Look for Plasmodium parasites.
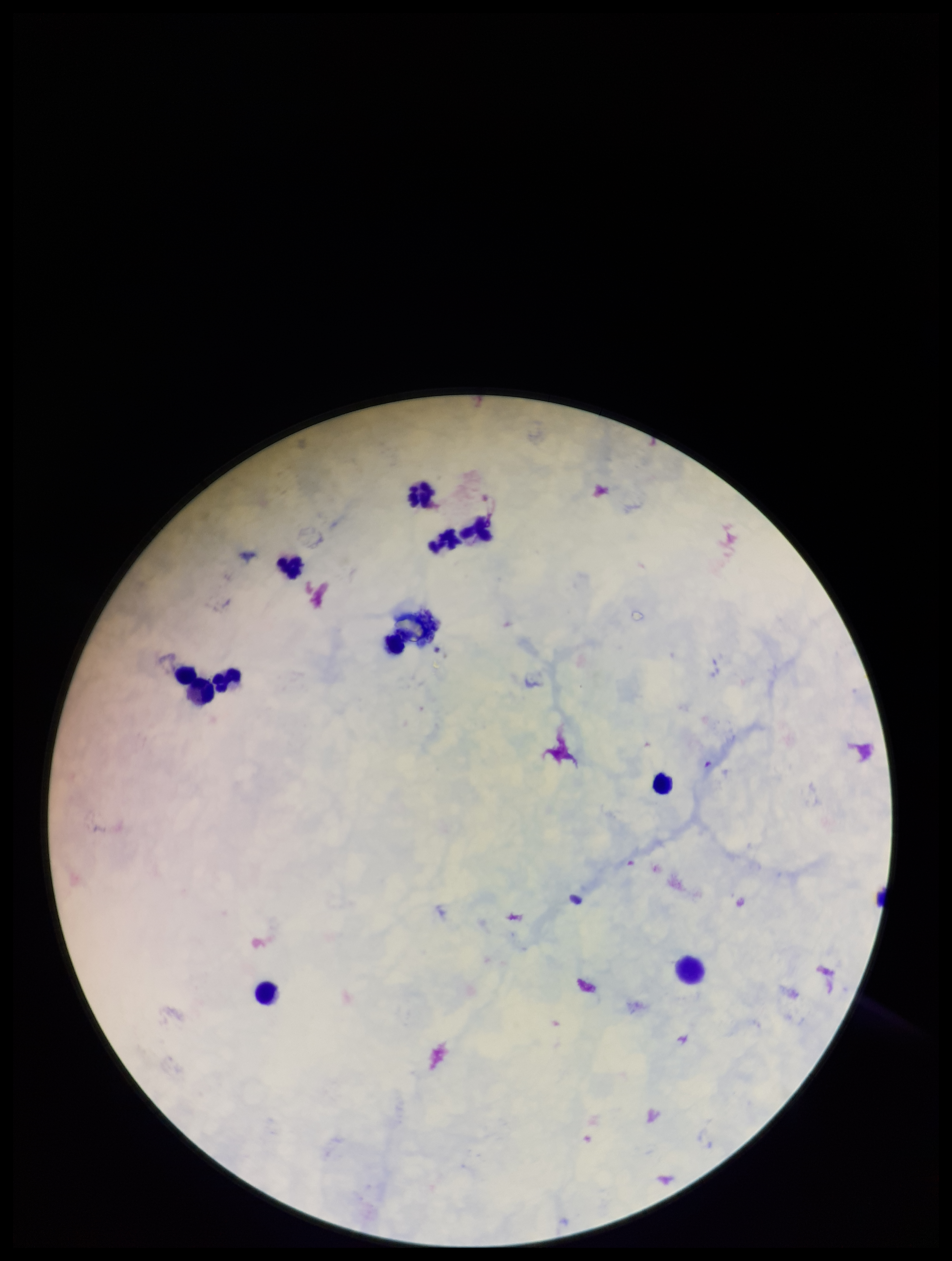
None identified.

Single field of view. Image is 952×1261 pixels. Photographed through the microscope eyepiece with a smartphone camera. Leukocyte count: 10. Preparation: thick blood smear. Parasite count: 0. Stained with Giemsa. Patient malaria status: negative.